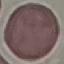

Malaria status: uninfected. Cell patch, automatically extracted from a larger field of view and resized to 64 × 64 pixels. Giemsa-stained preparation. Thin blood smear. Acquired by smartphone through the microscope eyepiece.